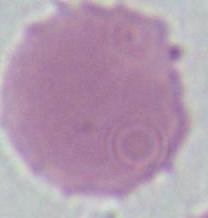
Summary:
  - Magnification: 1000x
  - Modality: micrograph
  - Identification: red blood cell